Assess this cell for malaria.
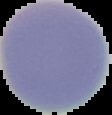
It is uninfected.

Image is 112×115 pixels. Cell region segmented out of the field of view; the surrounding area is masked to black. From a thin blood smear.